Classify this cell by malaria status.
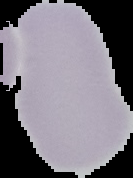

It is uninfected.

Summary:
  - Image type: segmented cell region on a black background
  - Image size: 133×178 pixels
  - Preparation: thin blood smear